Classify this cell by malaria status.
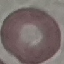

It is uninfected.

preparation: thin blood smear
capture: smartphone through the microscope eyepiece
stain: Giemsa
image_type: cell patch, automatically extracted from a larger field of view and resized to 64 × 64 pixels